Assess this cell for malaria.
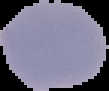

Uninfected.

Image is 109×91 pixels. From a thin blood film. Segmented cell region on a black background.